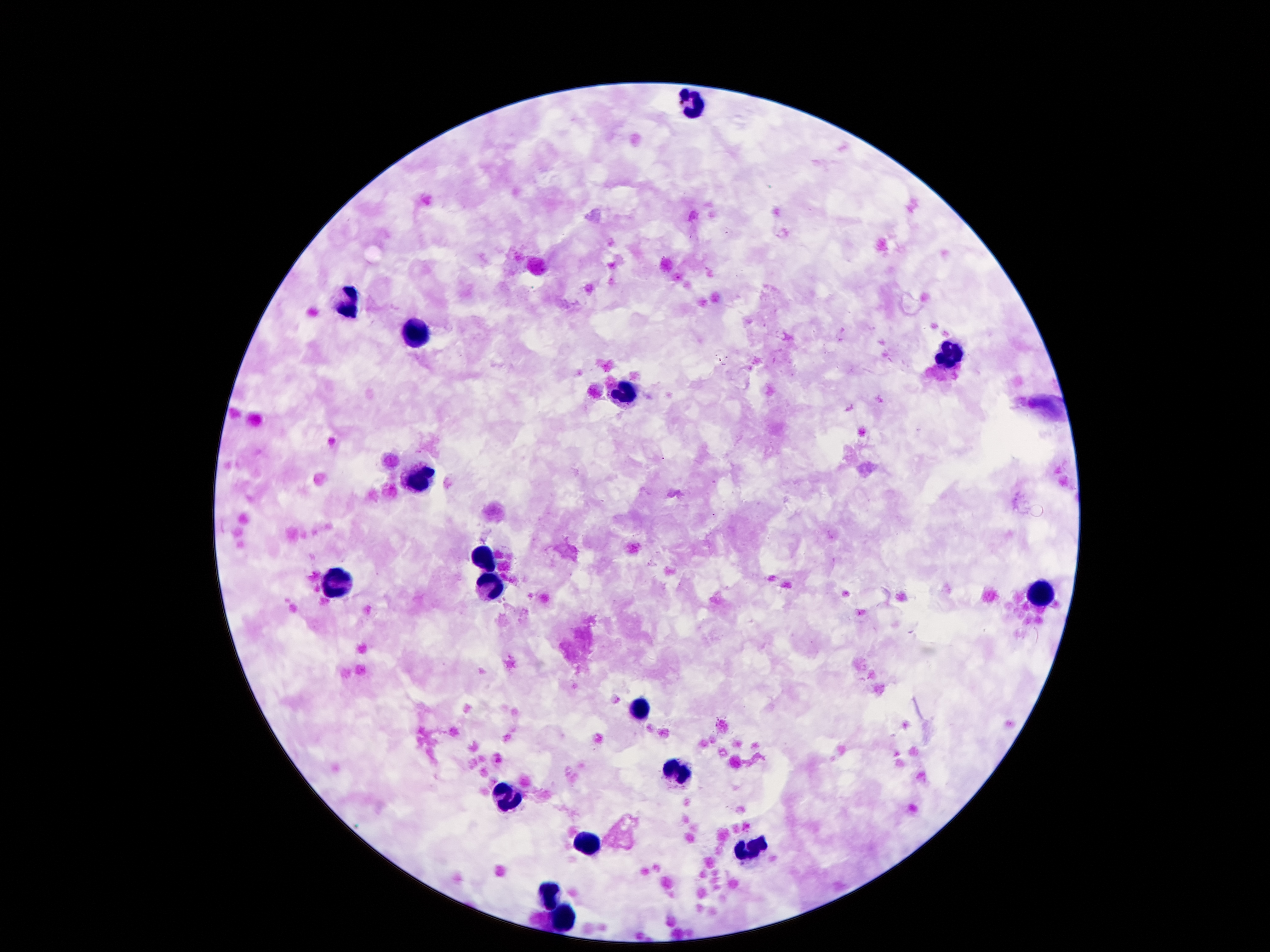 Approximate centers as (x, y) in pixels. Leukocyte locations: (693, 105), (343, 301), (416, 331), (948, 359), (621, 392), (420, 476), (481, 558), (339, 583), (488, 586), (1041, 590), (637, 707), (679, 770), (502, 800), (591, 845), (749, 852), (551, 898), (563, 917). Image is 1270×952 pixels. Photographed through the microscope eyepiece with a smartphone camera. Giemsa-stained preparation. Patient malaria status: positive for Plasmodium falciparum. Malaria parasites: not seen. Thick peripheral-blood smear. 100x magnification. One field from this slide.